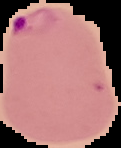

Summary:
  - Image size: 121×148 pixels
  - Image type: cell region segmented out of the field of view; surrounding area masked to black
  - Preparation: thin blood smear
  - Malaria status: parasitized